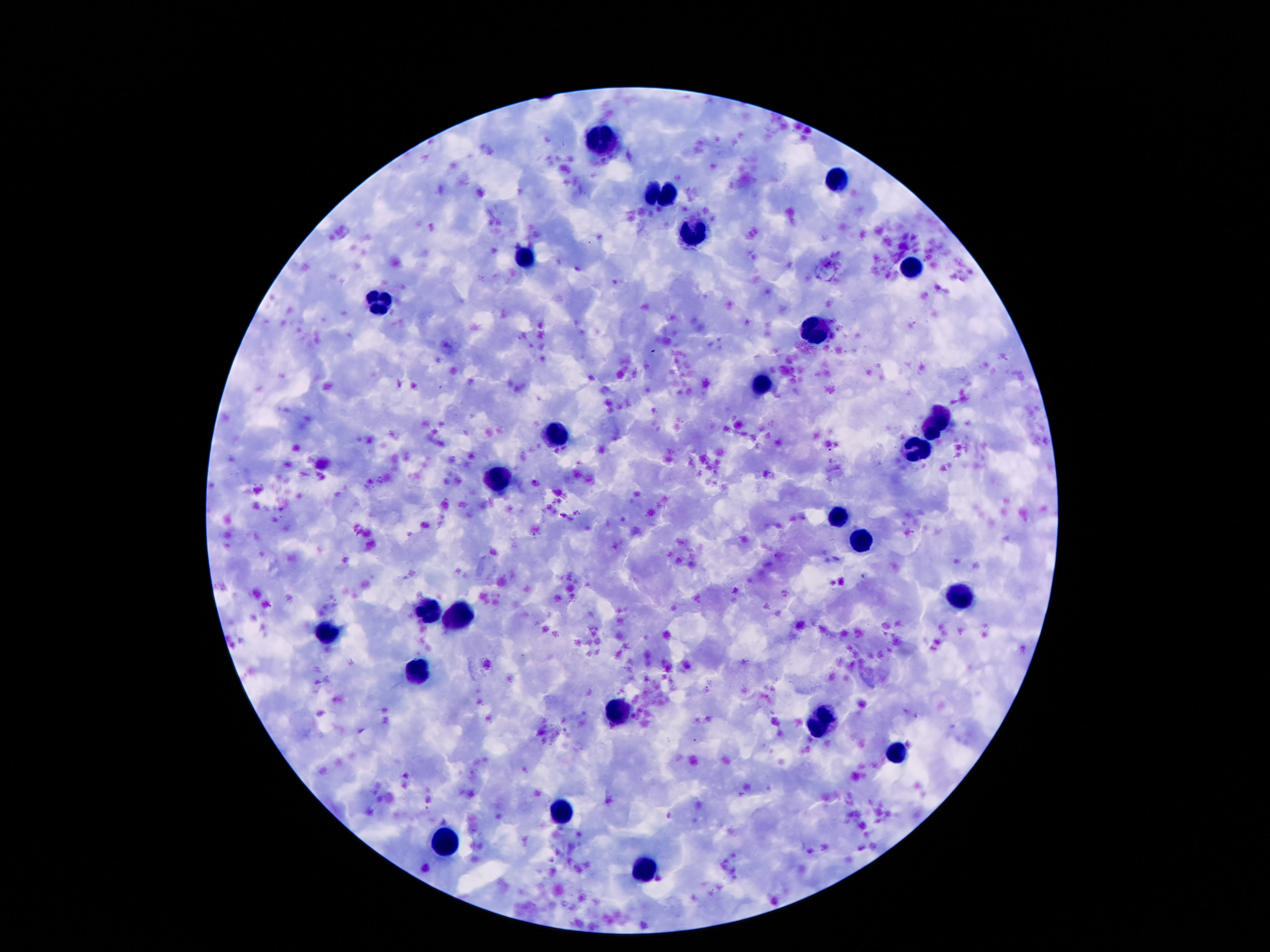 Approximate centers as (x, y) in pixels. Leukocyte locations: (603, 140), (839, 181), (648, 189), (671, 194), (692, 235), (526, 257), (911, 266), (378, 303), (818, 329), (761, 386), (937, 423), (556, 434), (913, 448), (501, 480), (837, 515), (857, 538), (958, 595), (431, 610), (456, 615), (329, 632), (417, 673), (618, 715), (821, 723), (894, 749), (560, 811), (450, 844), (646, 869). Smartphone photograph taken through the microscope eyepiece. Single field of view. Image is 1270×952 pixels. Giemsa-stained preparation. Patient malaria status: negative. Thick peripheral-blood smear. 100x magnification.